Assess the morphology of the erythrocytes.
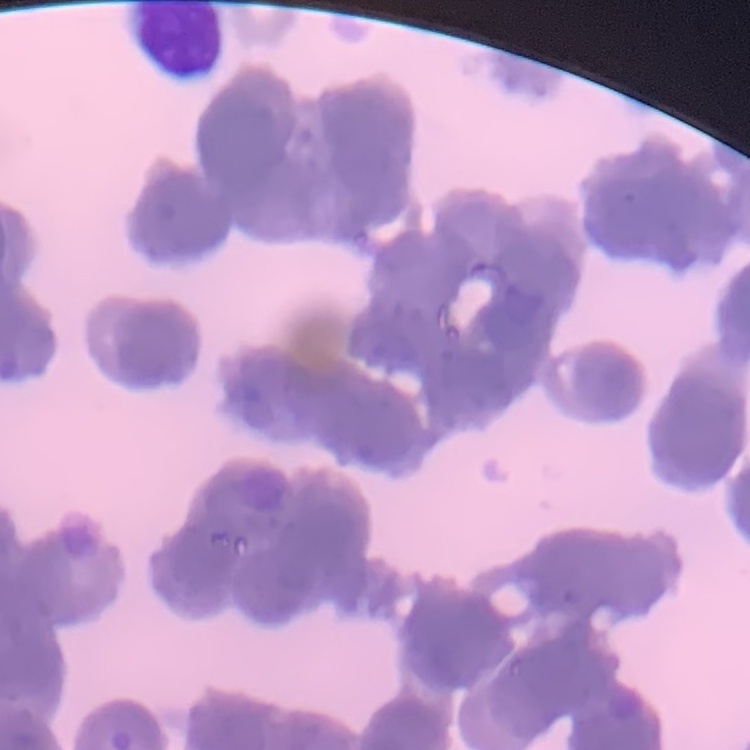
Rouleaux formation.

Stained with either Field's or Giemsa. Square crop of a larger photomicrograph. Thin peripheral smear.